Evaluate for Plasmodium parasites.
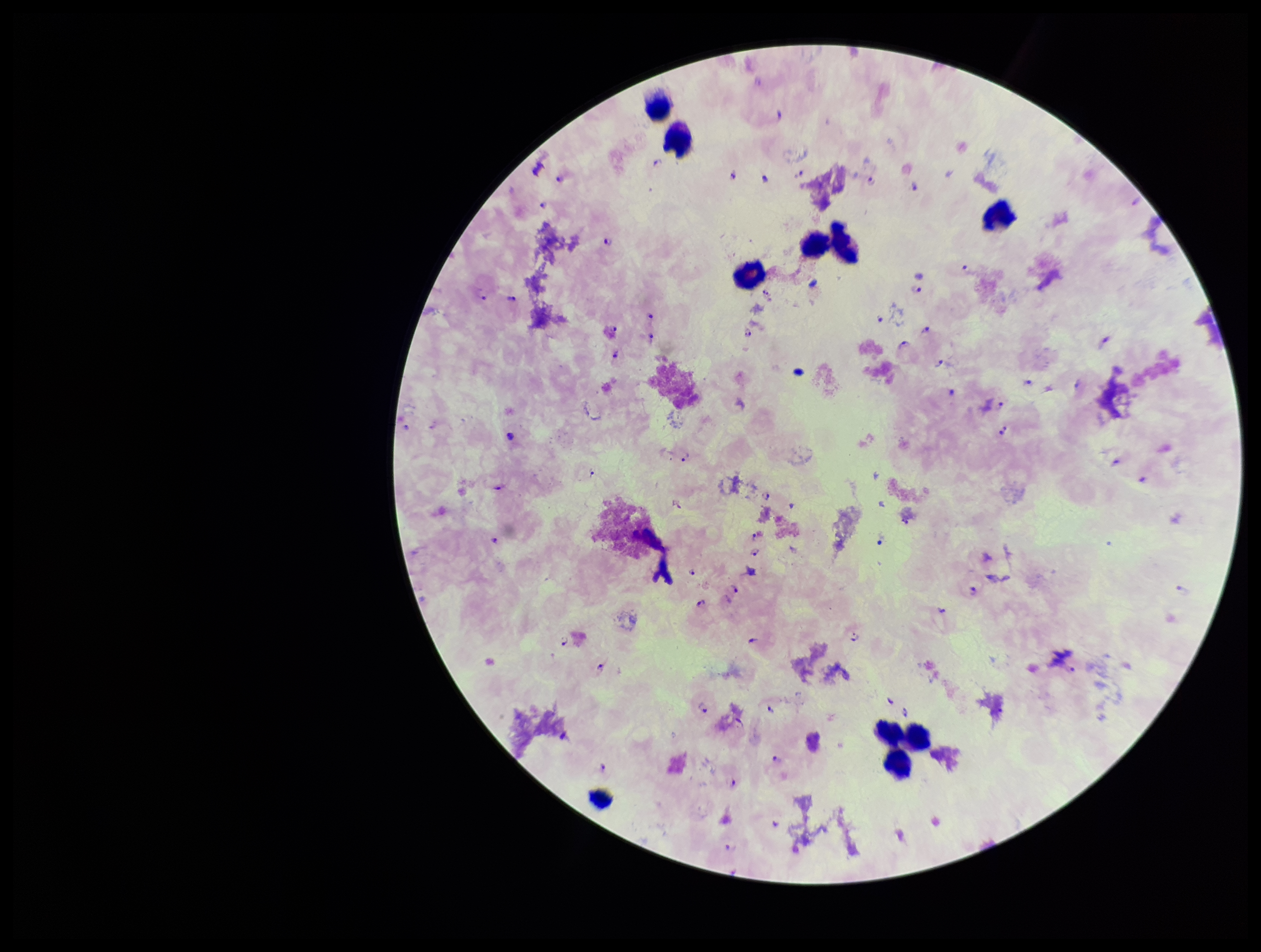
Seen.

Summary:
  - Field of view: one from this slide
  - Preparation: thick blood smear
  - Patient malaria status: infected
  - Capture: smartphone photograph through the microscope eyepiece
  - Species reported for this patient: Plasmodium falciparum
  - Leukocyte count: 9
  - Stain: Giemsa
  - Parasite count: 76
  - Image size: 1261×952 pixels